Assess the morphology of the erythrocytes.
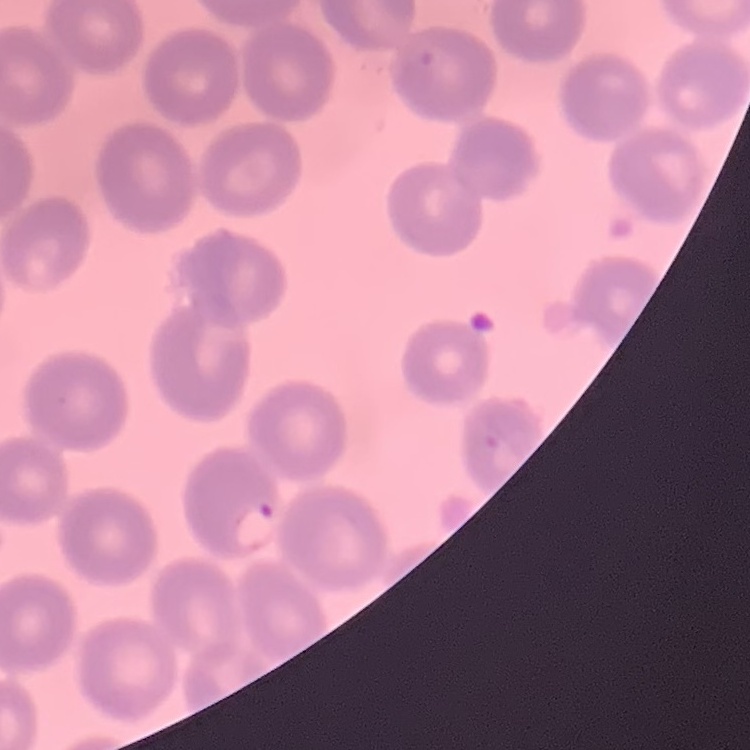

They show no rouleaux formation.

{
  "preparation": "thin peripheral smear",
  "image_type": "square crop of a larger photomicrograph",
  "stain": "Field's or Giemsa"
}